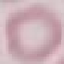

Result: negative for malaria parasites. Photographed with a smartphone camera at the microscope eyepiece. Thin smear of blood. Giemsa stain. Automatically extracted cell patch, resized to 64 × 64 pixels.